Identify the preparation type.
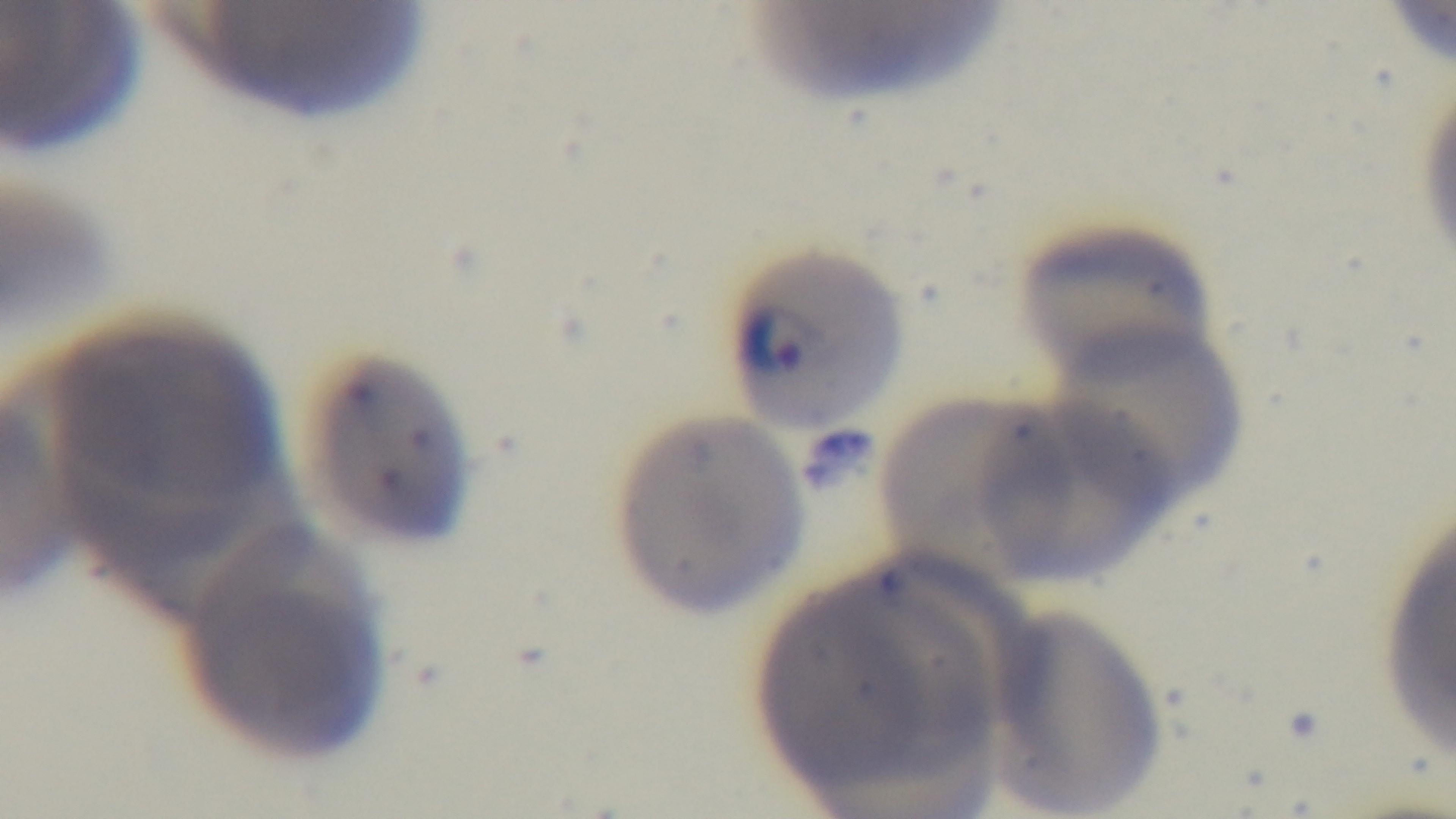

A thin smear.

capture = mounted 4K digital camera
objective = 100x oil immersion
stain = Giemsa
field of view = single
malaria status = positive
modality = light microscopy